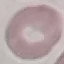
Summary:
  - Malaria status: uninfected
  - Preparation: thin smear
  - Stain: Giemsa
  - Image type: automatically extracted cell patch, resized to 64 × 64 pixels
  - Capture: smartphone through the microscope eyepiece